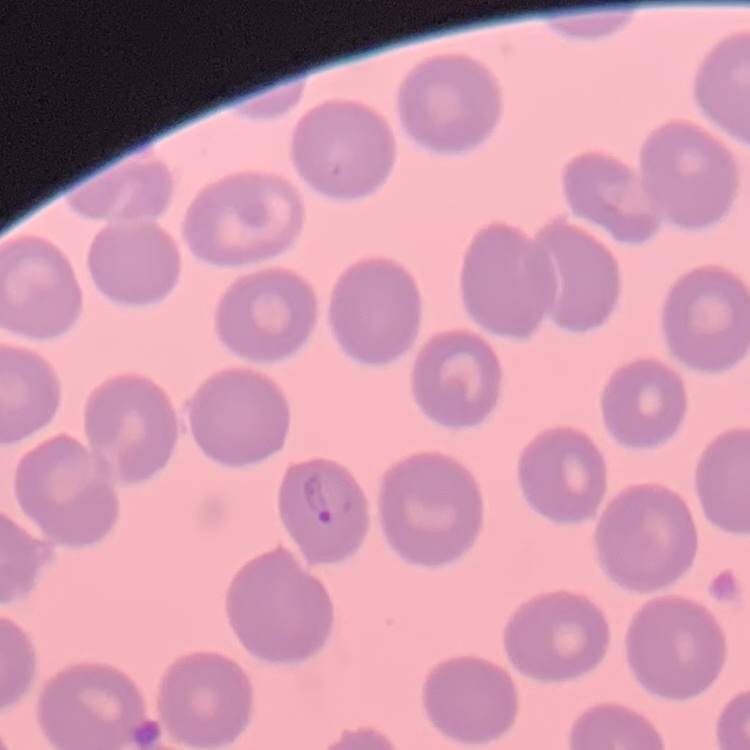 The erythrocytes show no rouleaux formation. Thin blood film. Stained with either Field's or Giemsa. One tile cut from a larger photomicrograph.